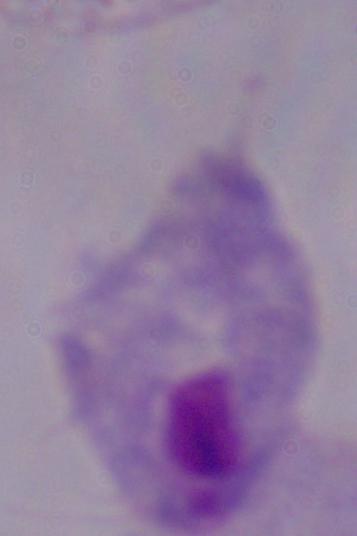
modality: photomicrograph
magnification: 1000x
identification: trichomonad